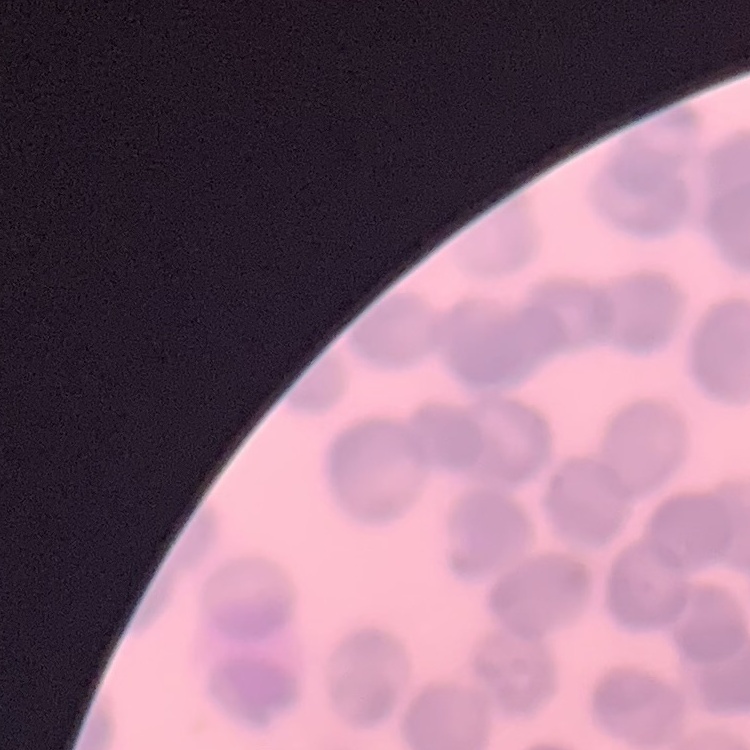

erythrocyte morphology = rouleaux formation
stain = Field's or Giemsa
preparation = thin peripheral smear
image type = one tile cut from a larger photomicrograph